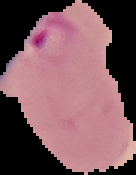

Summary:
  - Preparation: thin blood smear
  - Image size: 136×175 pixels
  - Image type: segmented cell region on a black background
  - Malaria status: parasitized